Identify the parasite.
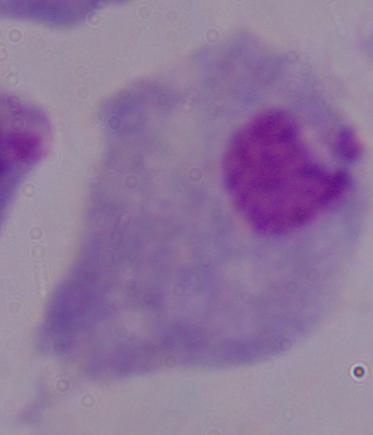
A trichomonad.

Captured at 1000x magnification. Micrograph.